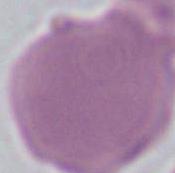
Summary:
  - Identification: red blood cell
  - Magnification: 1000x
  - Modality: photomicrograph